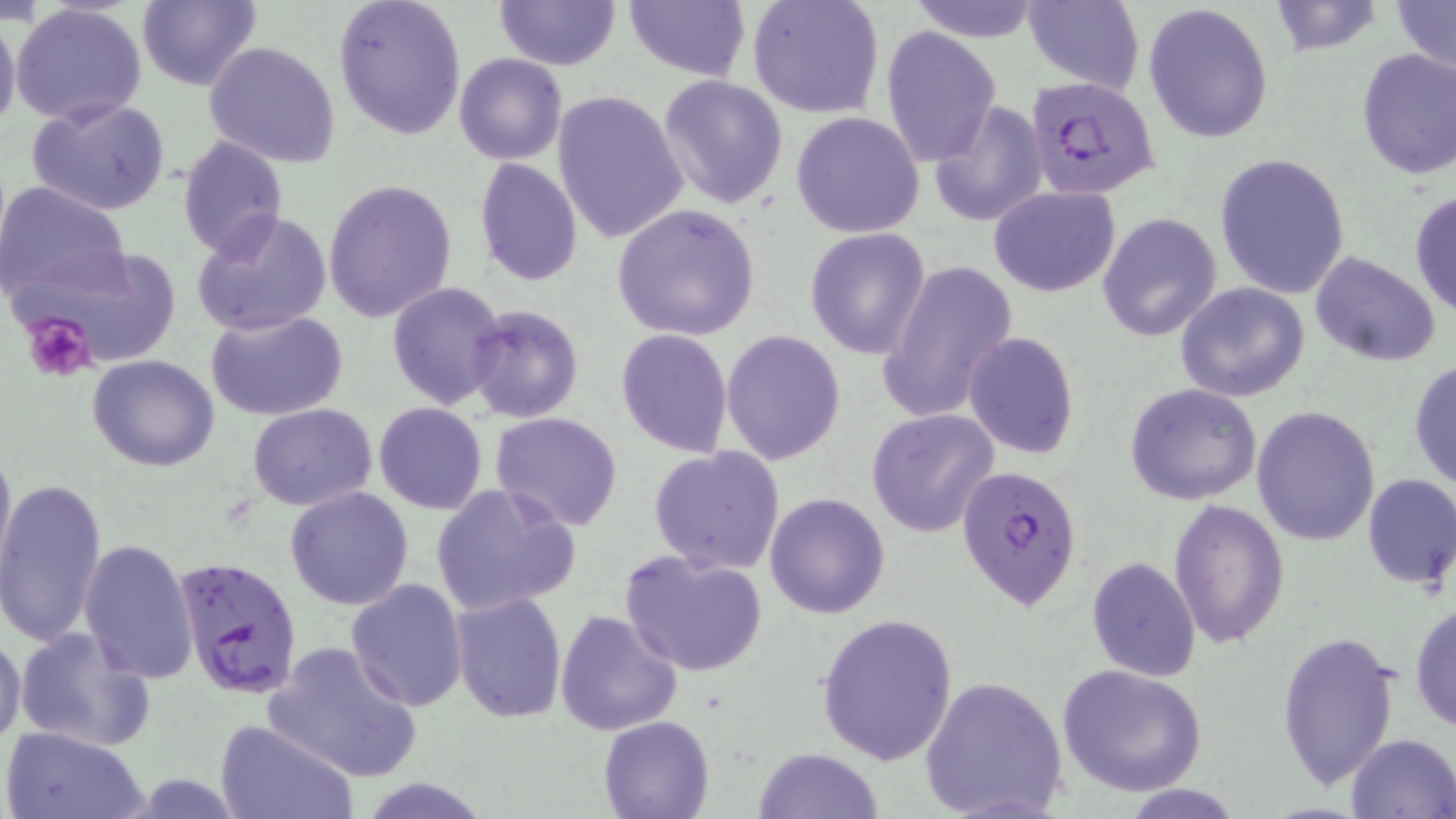

Approximate bounding boxes as (x1, y1, x2, y2) in pixels. Plasmodium falciparum-infected red blood cell locations: (1028, 69, 1163, 205), (956, 463, 1084, 612), (174, 556, 302, 698). Platelet locations: (20, 315, 98, 383). Uninfected red blood cell locations: (332, 0, 467, 141), (495, 0, 620, 71), (622, 0, 749, 82), (746, 0, 885, 121), (1022, 0, 1144, 93), (1263, 0, 1386, 56), (135, 1, 262, 90), (1391, 1, 1455, 82), (904, 2, 1045, 42), (1143, 2, 1275, 144), (10, 5, 148, 129), (0, 8, 21, 140), (879, 26, 1000, 165), (203, 41, 341, 169), (1355, 46, 1456, 180), (454, 52, 567, 166), (657, 75, 789, 211), (552, 89, 689, 243), (26, 94, 173, 219), (929, 101, 1047, 228), (790, 110, 926, 239), (176, 136, 288, 261), (1213, 151, 1353, 298), (474, 156, 585, 288), (321, 179, 459, 323), (2, 180, 131, 305), (988, 185, 1121, 298), (1408, 188, 1456, 319), (612, 203, 760, 342), (191, 210, 334, 337), (1096, 211, 1222, 342), (804, 227, 933, 361), (13, 249, 182, 376), (1309, 252, 1442, 366), (877, 258, 1019, 422), (385, 281, 507, 409), (1176, 282, 1311, 402), (464, 304, 583, 423), (207, 311, 348, 422), (615, 329, 734, 458), (721, 329, 847, 467), (963, 330, 1080, 461), (87, 354, 221, 474), (1409, 358, 1456, 491), (1123, 381, 1263, 505), (373, 402, 487, 514), (248, 403, 377, 511), (1251, 405, 1382, 546), (867, 408, 1000, 537), (490, 410, 624, 531), (0, 435, 15, 576), (648, 445, 786, 574), (1361, 472, 1456, 591), (0, 474, 107, 653), (431, 481, 582, 617), (285, 485, 415, 610), (764, 492, 891, 618), (1168, 499, 1290, 647), (79, 537, 199, 682), (619, 549, 769, 676), (1086, 556, 1200, 682), (346, 578, 469, 711), (449, 591, 567, 724), (1409, 596, 1456, 733), (553, 609, 682, 737), (817, 613, 957, 766), (15, 626, 155, 751), (0, 630, 26, 752), (1275, 631, 1400, 791), (265, 641, 422, 784), (1057, 663, 1208, 797), (919, 675, 1068, 819), (598, 715, 714, 819), (214, 717, 358, 819), (2, 726, 149, 819), (1345, 733, 1456, 818), (754, 747, 883, 819), (361, 777, 492, 818), (1114, 782, 1248, 818). Slide-level diagnosis: Plasmodium falciparum. Light microscopy. Thin blood smear. May-Grünwald-Giemsa-stained preparation. Image is 1456×819 pixels. 1000x magnification. Single field of view.